Locate every P. falciparum parasite and give its life-cycle stage, and locate every leukocyte and any debris.
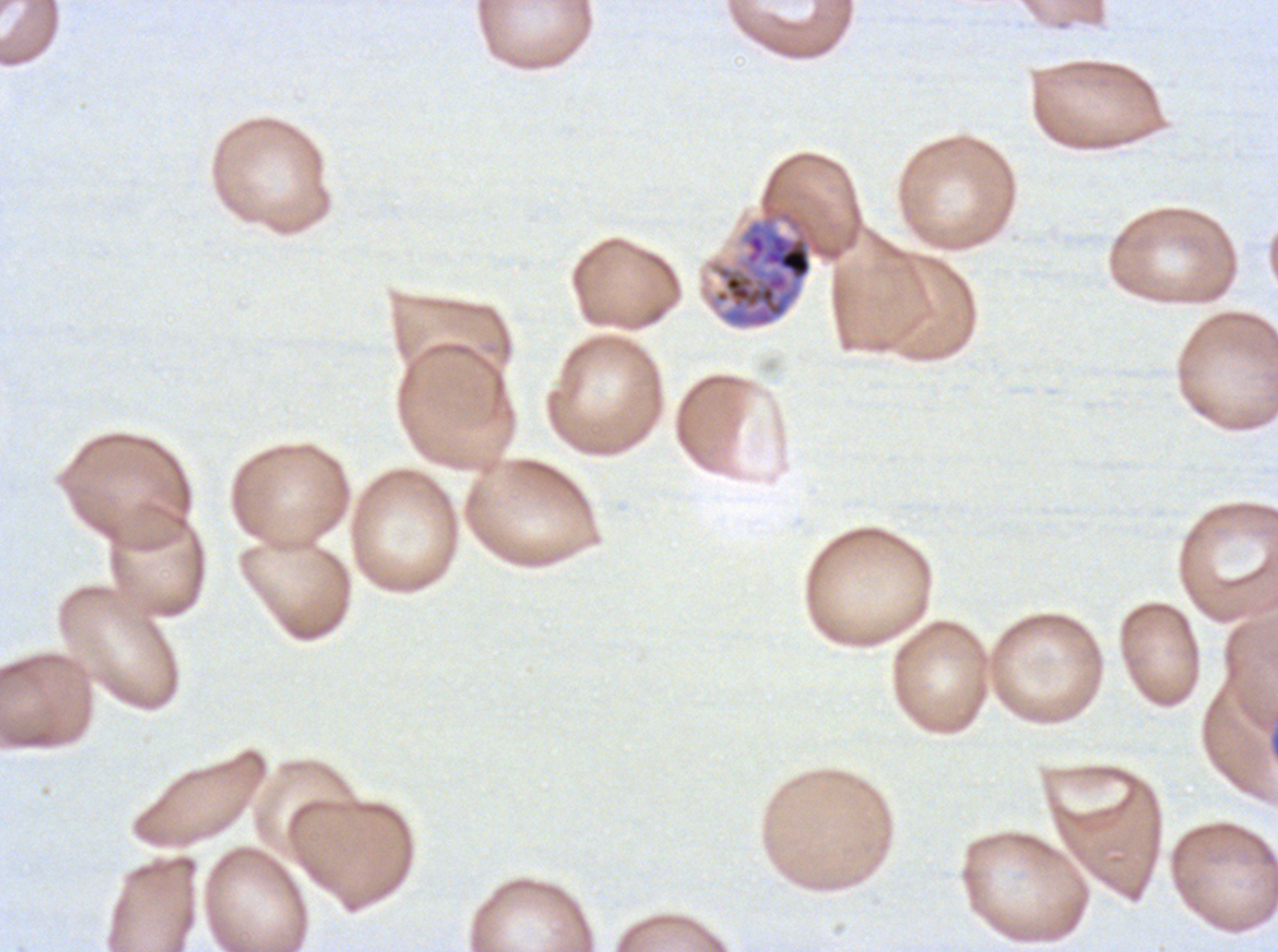
Approximate bounding rectangles given as corner coordinates in pixels from the top-left.
Late schizonts: (x1=714, y1=215, x2=813, y2=328).
No rings, late-ring/early-trophozoite forms, mid trophozoites, late trophozoites, early schizonts, segmenters, gametocytes, leukocytes, or debris observed.

specimen = P. falciparum from a patient in The Gambia, cultured ex vivo for 24 to 48 hours
stain = Giemsa
field of view = one sub-image of a larger composite
preparation = thin blood smear
image size = 1278×952 pixels